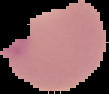
malaria status = uninfected
preparation = thin blood film
image type = segmented cell region with the area outside set to black
image size = 109×94 pixels